Comment on the morphology of the red blood cells.
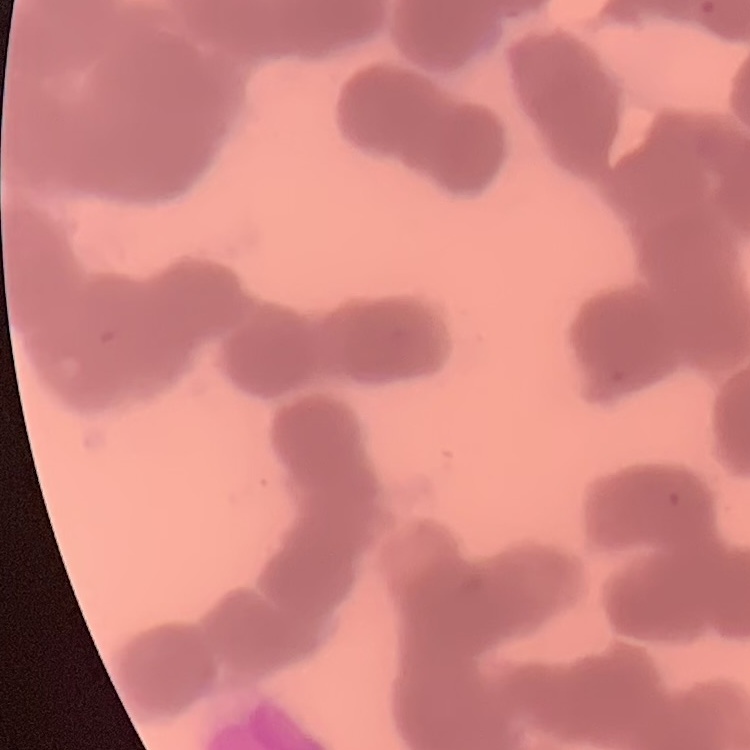
Rouleaux formation.

image type = one tile cut from a larger photomicrograph
preparation = thin blood smear
stain = Field's or Giemsa